Report the malaria status of this cell.
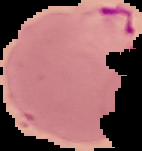
Parasitized.

Summary:
  - Preparation: thin blood film
  - Image type: segmented cell region on a black background
  - Image size: 142×151 pixels